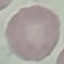
Summary:
  - Result: no malaria parasites seen
  - Preparation: thin blood smear
  - Stain: Giemsa
  - Image type: automatically extracted cell patch, resized to 64 × 64 pixels
  - Capture: smartphone through the microscope eyepiece